Assess the morphology of the red blood cells.
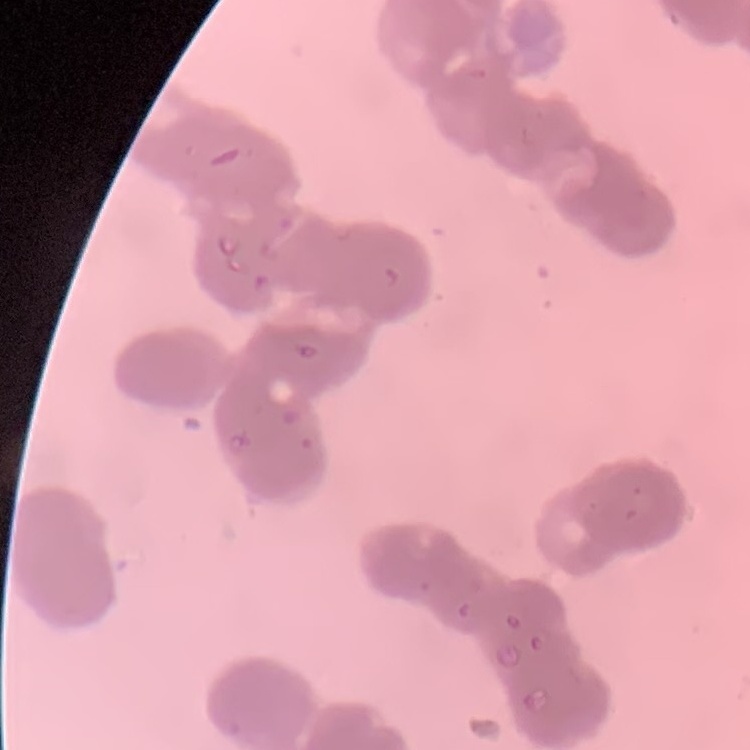
They show rouleaux formation.

preparation = thin blood film
stain = Field's or Giemsa
image type = one tile cut from a larger photomicrograph